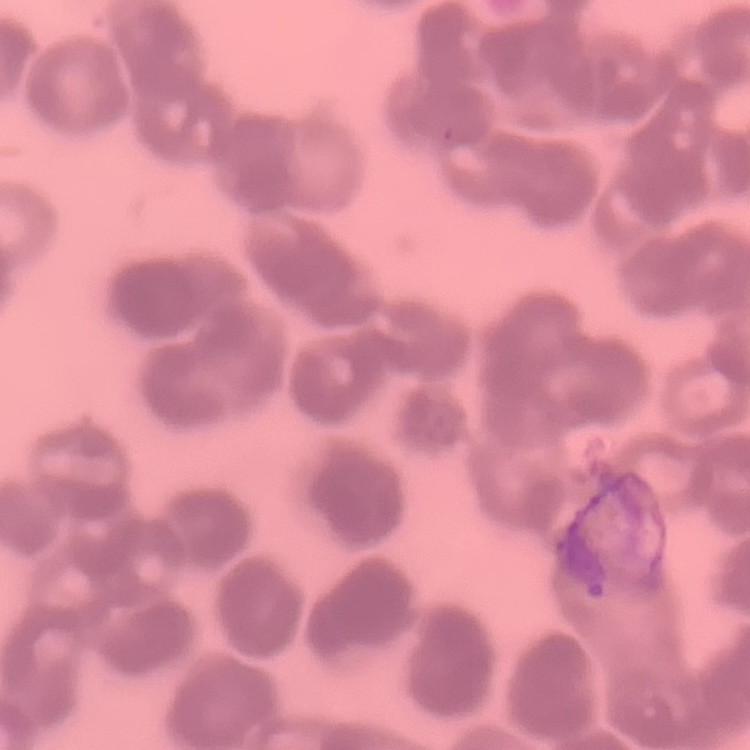

erythrocyte morphology = rouleaux formation
stain = Field's or Giemsa
image type = one tile cut from a larger photomicrograph
preparation = thin blood film